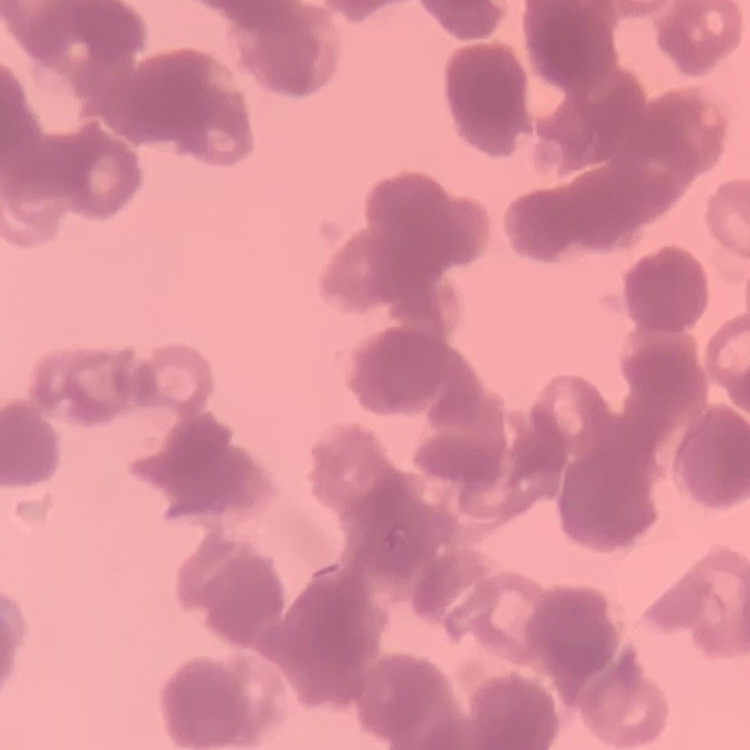

The red blood cells show rouleaux formation. Thin blood film. Square crop of a larger photomicrograph. Field's or Giemsa stain.